Describe the morphology of the erythrocytes.
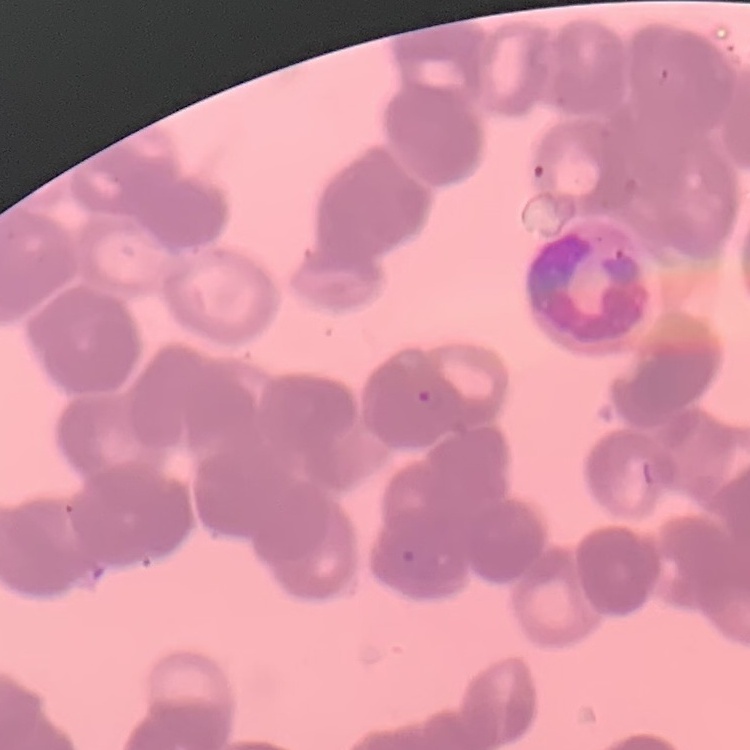

They show rouleaux formation.

Square crop of a larger photomicrograph. Field's or Giemsa stain. Thin blood smear.